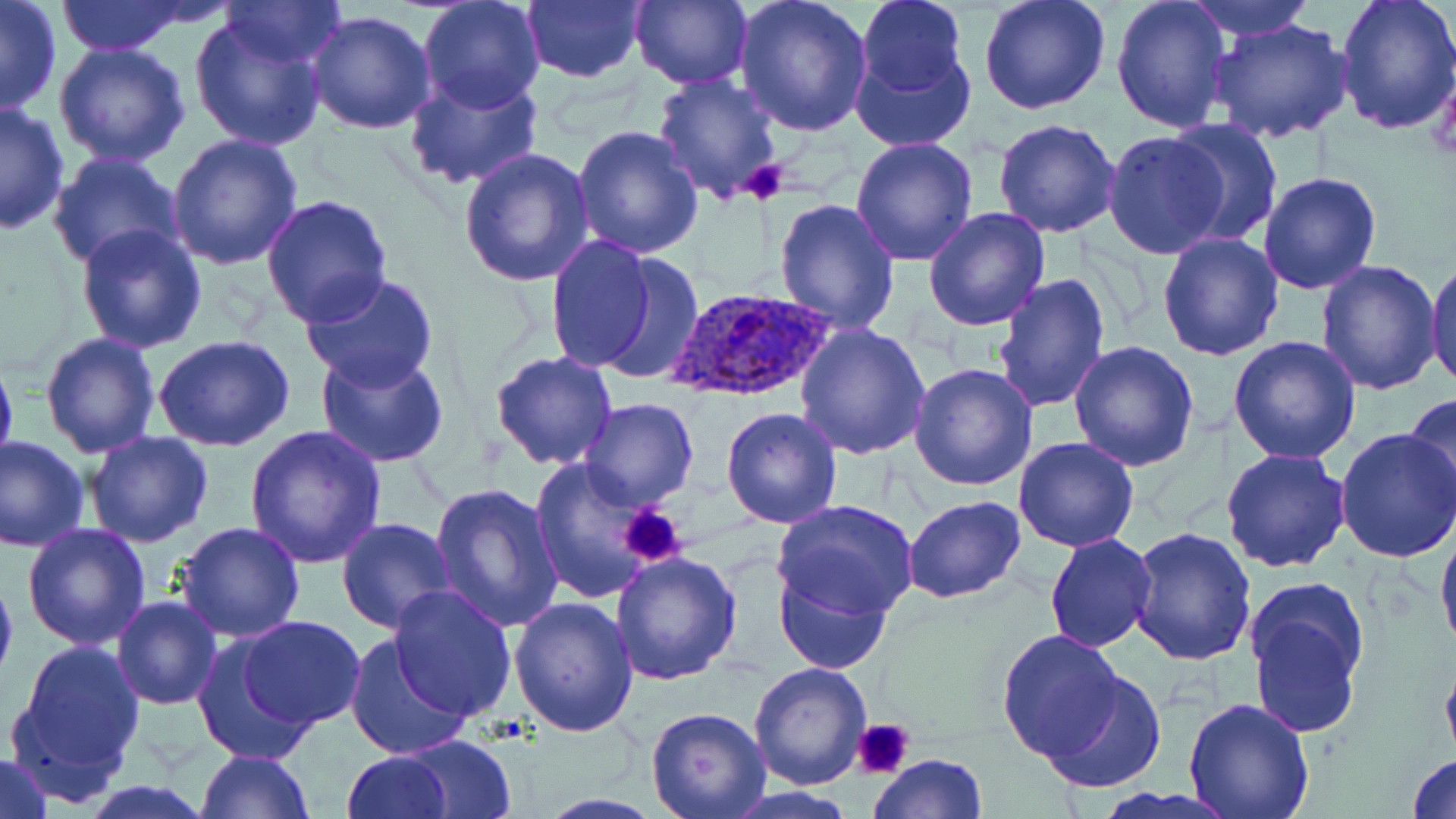
slide-level diagnosis = Plasmodium ovale
modality = optical microscopy
field of view = one of a larger specimen
platelet locations = approximate bounding boxes as [x1, y1, x2, y2] in pixels: [742, 158, 790, 205], [619, 504, 689, 569], [854, 716, 917, 778]
preparation = thin blood film
Plasmodium ovale-infected red blood cell locations = approximate bounding boxes as [x1, y1, x2, y2] in pixels: [666, 288, 837, 403]
magnification = 1000x
image size = 1456×819 pixels
uninfected red blood cell locations = approximate bounding boxes as [x1, y1, x2, y2] in pixels: [0, 0, 62, 117], [56, 0, 188, 55], [218, 0, 349, 69], [520, 0, 647, 84], [627, 0, 753, 89], [732, 0, 875, 137], [854, 0, 968, 97], [978, 0, 1111, 116], [1111, 0, 1233, 136], [1182, 0, 1317, 41], [1333, 0, 1456, 136], [417, 1, 546, 114], [306, 11, 437, 135], [189, 13, 327, 152], [1205, 16, 1355, 146], [53, 42, 193, 168], [849, 44, 976, 152], [404, 71, 544, 191], [652, 74, 783, 199], [0, 102, 70, 235], [1166, 117, 1282, 246], [993, 118, 1123, 238], [571, 126, 703, 258], [1102, 130, 1230, 261], [167, 132, 303, 269], [851, 136, 980, 265], [459, 146, 594, 287], [46, 151, 186, 275], [1260, 173, 1383, 294], [260, 194, 393, 327], [775, 197, 899, 336], [922, 206, 1052, 331], [75, 222, 208, 354], [1157, 230, 1287, 360], [546, 235, 659, 373], [592, 254, 704, 387], [1424, 255, 1455, 392], [1315, 261, 1442, 395], [992, 272, 1108, 414], [299, 273, 442, 391], [794, 321, 932, 460], [40, 333, 162, 459], [1229, 334, 1362, 464], [154, 336, 297, 453], [1068, 339, 1200, 470], [0, 346, 18, 475], [316, 349, 449, 468], [490, 351, 619, 470], [909, 362, 1039, 491], [1403, 393, 1456, 511], [578, 399, 700, 513], [721, 407, 843, 529], [244, 424, 386, 567], [1336, 425, 1456, 562], [85, 431, 216, 548], [0, 435, 90, 552], [1014, 436, 1142, 551], [1221, 447, 1350, 573], [530, 461, 658, 603], [430, 485, 563, 634], [903, 496, 1027, 603], [772, 499, 920, 621], [334, 518, 456, 635], [176, 520, 307, 641], [21, 522, 151, 649], [1436, 522, 1456, 659], [1129, 528, 1257, 668], [1044, 534, 1158, 653], [611, 550, 743, 685], [774, 566, 892, 675], [0, 568, 18, 690], [1244, 578, 1371, 738], [388, 584, 517, 721], [112, 595, 222, 710], [510, 597, 639, 738], [239, 616, 364, 729], [997, 628, 1125, 760], [194, 631, 315, 760], [342, 635, 471, 764], [9, 640, 146, 787], [1439, 654, 1456, 769], [747, 662, 873, 789], [1038, 672, 1165, 796], [1182, 698, 1315, 819], [645, 708, 770, 819], [401, 736, 516, 818], [195, 750, 313, 818], [343, 750, 450, 818], [1, 751, 54, 819], [1407, 751, 1456, 819], [869, 754, 987, 818], [534, 793, 667, 818]
stain = May-Grünwald-Giemsa